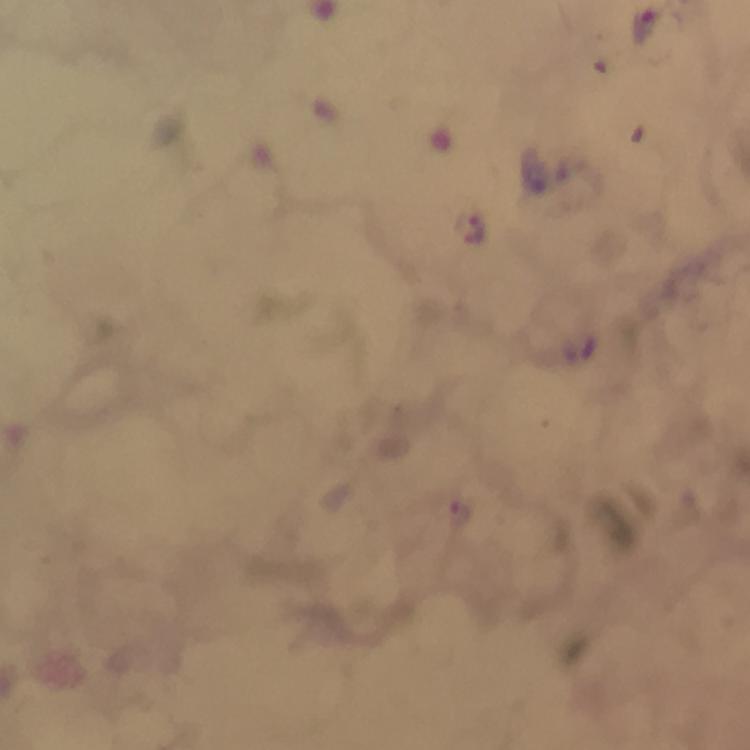

immersion_oil: used
image_size: 750×750 pixels
stain: Giemsa
cropped_from: a single field of view
context: from a diagnostic examination for malaria
magnification: 100x
capture: smartphone camera through the microscope
preparation: thick blood film
malaria_parasite_locations: 'approximate object centers, in pixels from the top-left corner: (x=648, y=26), (x=477, y=228), (x=457, y=515)'